Give the preparation type.
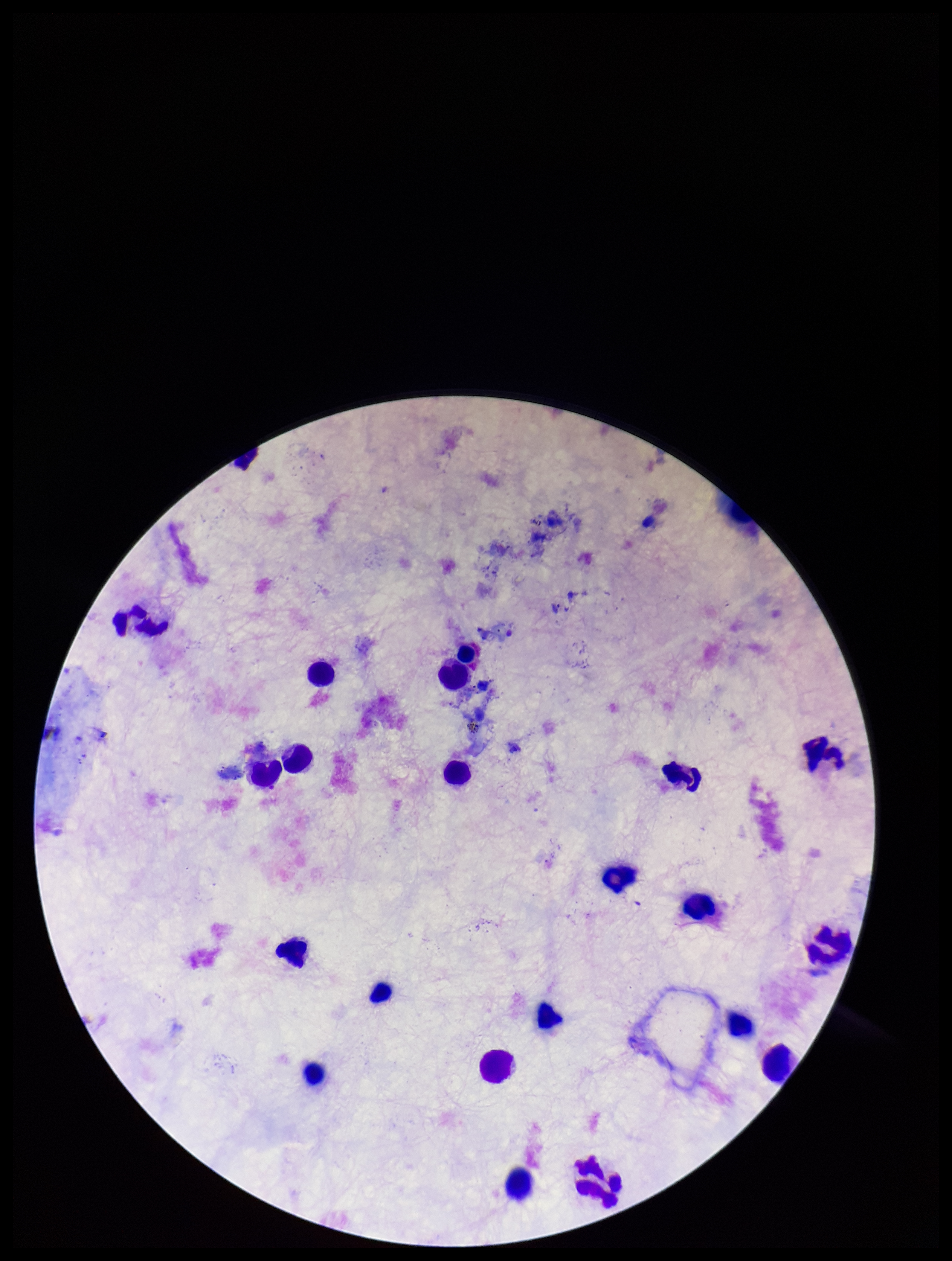

It is a thick blood smear.

Summary:
  - Stain: Giemsa
  - Plasmodium parasites: none identified
  - Field of view: single
  - Image size: 952×1261 pixels
  - Patient malaria status: negative
  - Leukocyte count: 21
  - Parasite count: 0
  - Capture: smartphone photograph through the microscope eyepiece